Report the malaria status of this cell.
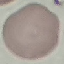

Uninfected.

Thin smear of blood. Acquired by smartphone through the microscope eyepiece. Giemsa-stained preparation. Cell patch, automatically extracted from a larger field of view and resized to 64 × 64 pixels.